Report the malaria status of this cell.
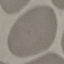
It is uninfected.

image type = automatically extracted cell patch, resized to 64 × 64 pixels
preparation = thin smear
stain = Giemsa
capture = smartphone camera at the microscope eyepiece